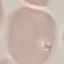
Summary:
  - Malaria status: uninfected
  - Preparation: thin blood film
  - Stain: Giemsa
  - Image type: cell patch, automatically extracted from a larger field of view and resized to 64 × 64 pixels
  - Capture: smartphone through the microscope eyepiece